Assess this cell for malaria.
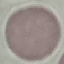
Uninfected.

Cell patch, automatically extracted from a larger field of view and resized to 64 × 64 pixels. Thin smear of blood. Photographed with a smartphone camera at the microscope eyepiece. Giemsa stain.